Identify the parasite.
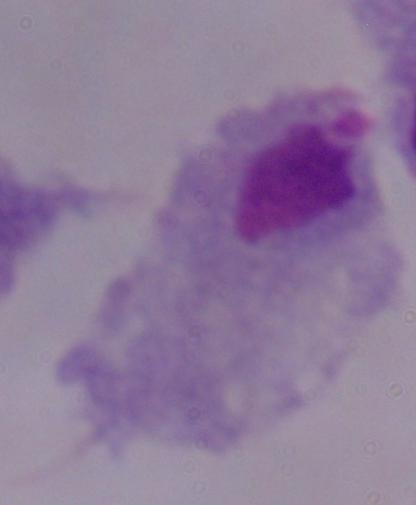
A trichomonad.

Photomicrograph. 1000x magnification.